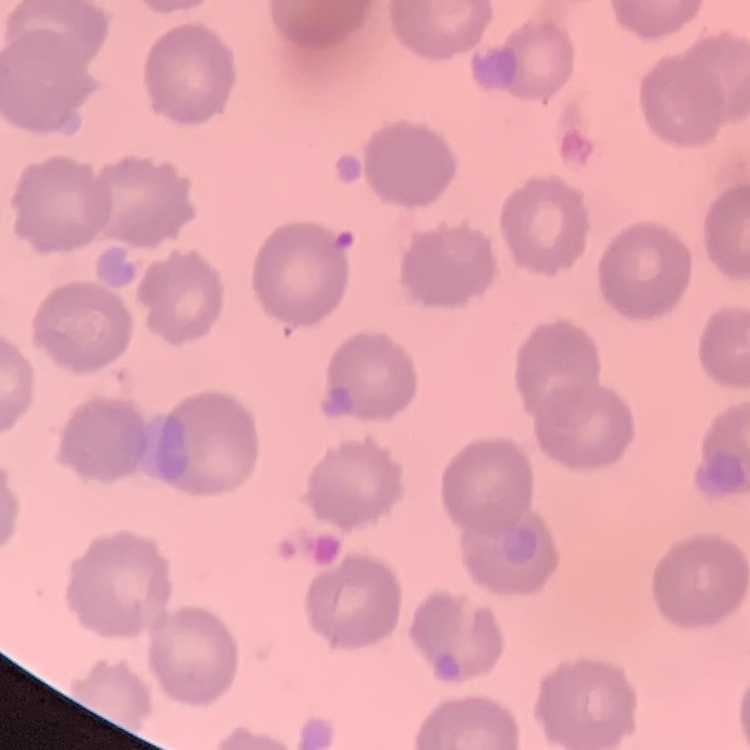
erythrocyte morphology = no rouleaux formation
stain = Field's or Giemsa
image type = square crop of a larger photomicrograph
preparation = thin blood smear